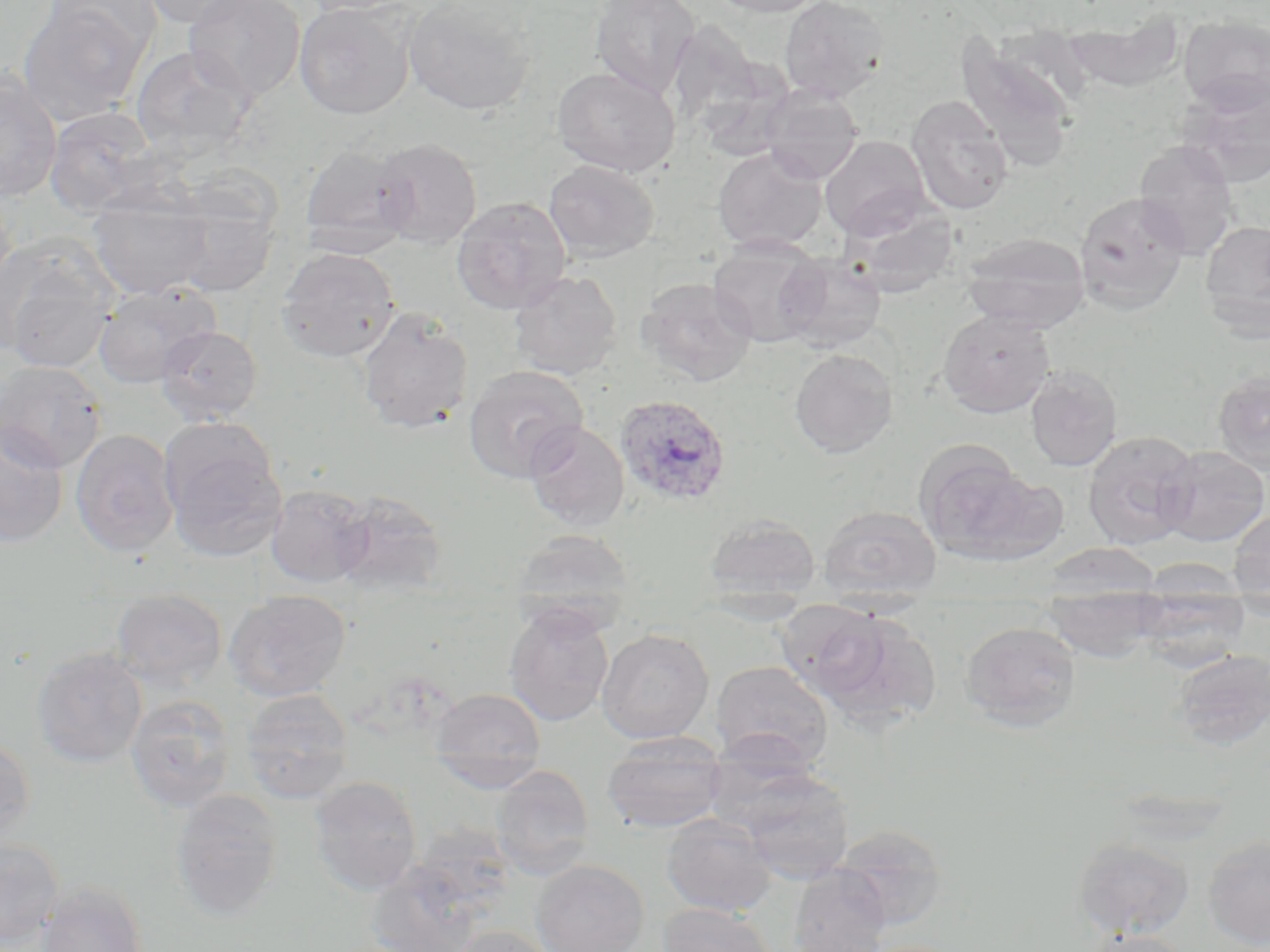
slide_level_diagnosis: Plasmodium ovale
uninfected_red_blood_cell_locations: 'approximate bounding boxes as [x1, y1, x2, y2] in pixels: [17, 0, 150, 124], [40, 0, 160, 61], [136, 0, 258, 28], [183, 0, 305, 103], [297, 0, 421, 16], [403, 0, 538, 116], [589, 0, 701, 100], [708, 0, 828, 17], [779, 0, 889, 103], [294, 2, 416, 119], [1061, 13, 1185, 90], [1178, 16, 1270, 111], [665, 20, 768, 136], [954, 35, 1079, 170], [130, 45, 255, 159], [553, 66, 680, 178], [0, 68, 63, 203], [1179, 75, 1270, 187], [759, 87, 864, 183], [906, 94, 1014, 216], [44, 106, 159, 216], [820, 134, 932, 240], [373, 137, 482, 248], [1133, 139, 1240, 259], [299, 142, 416, 252], [713, 146, 828, 253], [543, 159, 660, 261], [88, 184, 216, 300], [0, 190, 17, 301], [169, 191, 280, 297], [1074, 191, 1189, 314], [451, 196, 572, 314], [842, 205, 961, 299], [1200, 220, 1270, 336], [960, 232, 1091, 333], [0, 235, 118, 371], [708, 240, 827, 347], [276, 247, 401, 362], [776, 254, 887, 352], [508, 270, 623, 380], [635, 277, 757, 387], [92, 283, 219, 388], [356, 308, 474, 435], [938, 310, 1055, 417], [155, 324, 263, 425], [789, 348, 897, 458], [0, 360, 107, 472], [463, 364, 589, 483], [1025, 365, 1122, 471], [1213, 370, 1270, 475], [160, 421, 286, 561], [525, 421, 629, 531], [0, 425, 68, 548], [70, 428, 179, 557], [1082, 430, 1200, 549], [1158, 445, 1270, 546], [915, 446, 1057, 565], [265, 484, 373, 586], [331, 490, 447, 595], [819, 505, 942, 598], [1228, 507, 1270, 606], [703, 514, 822, 601], [510, 529, 637, 624], [1040, 542, 1164, 599], [1043, 586, 1166, 661], [1133, 589, 1250, 666], [224, 593, 352, 702], [110, 594, 228, 691], [504, 604, 614, 726], [797, 606, 941, 725], [960, 621, 1082, 730], [596, 629, 714, 743], [32, 648, 148, 767], [1170, 648, 1270, 751], [710, 660, 833, 770], [430, 687, 546, 784], [241, 689, 354, 804], [126, 694, 236, 813], [602, 733, 728, 834], [702, 734, 827, 832], [0, 737, 37, 849], [490, 764, 595, 878], [736, 768, 854, 882], [308, 776, 423, 896], [170, 789, 284, 921], [661, 813, 776, 917], [832, 824, 948, 928], [1202, 835, 1270, 950], [1072, 836, 1195, 938], [0, 837, 65, 949], [366, 856, 495, 952], [530, 860, 649, 952], [788, 866, 892, 952], [36, 882, 149, 952], [659, 903, 777, 952], [449, 925, 558, 952], [1080, 930, 1195, 952]'
stain: May-Grünwald-Giemsa
modality: optical microscopy
preparation: thin blood film
field_of_view: single
plasmodium_ovale_infected_red_blood_cell_locations: 'approximate bounding boxes as [x1, y1, x2, y2] in pixels: [614, 393, 733, 509]'
magnification: 1000x
image_size: 1270×952 pixels